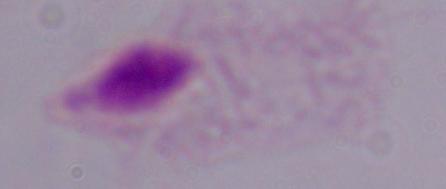
identification = trichomonad
modality = micrograph
magnification = 1000x